Report the malaria status of this cell.
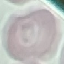

Uninfected.

image_type: automatically extracted cell patch, resized to 64 × 64 pixels
capture: smartphone through the microscope eyepiece
stain: Giemsa
preparation: thin smear